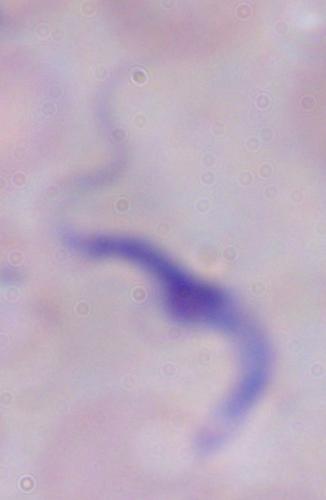
identification = trypanosome
modality = photomicrograph
magnification = 1000x